Locate every blood parasite and identify its species.
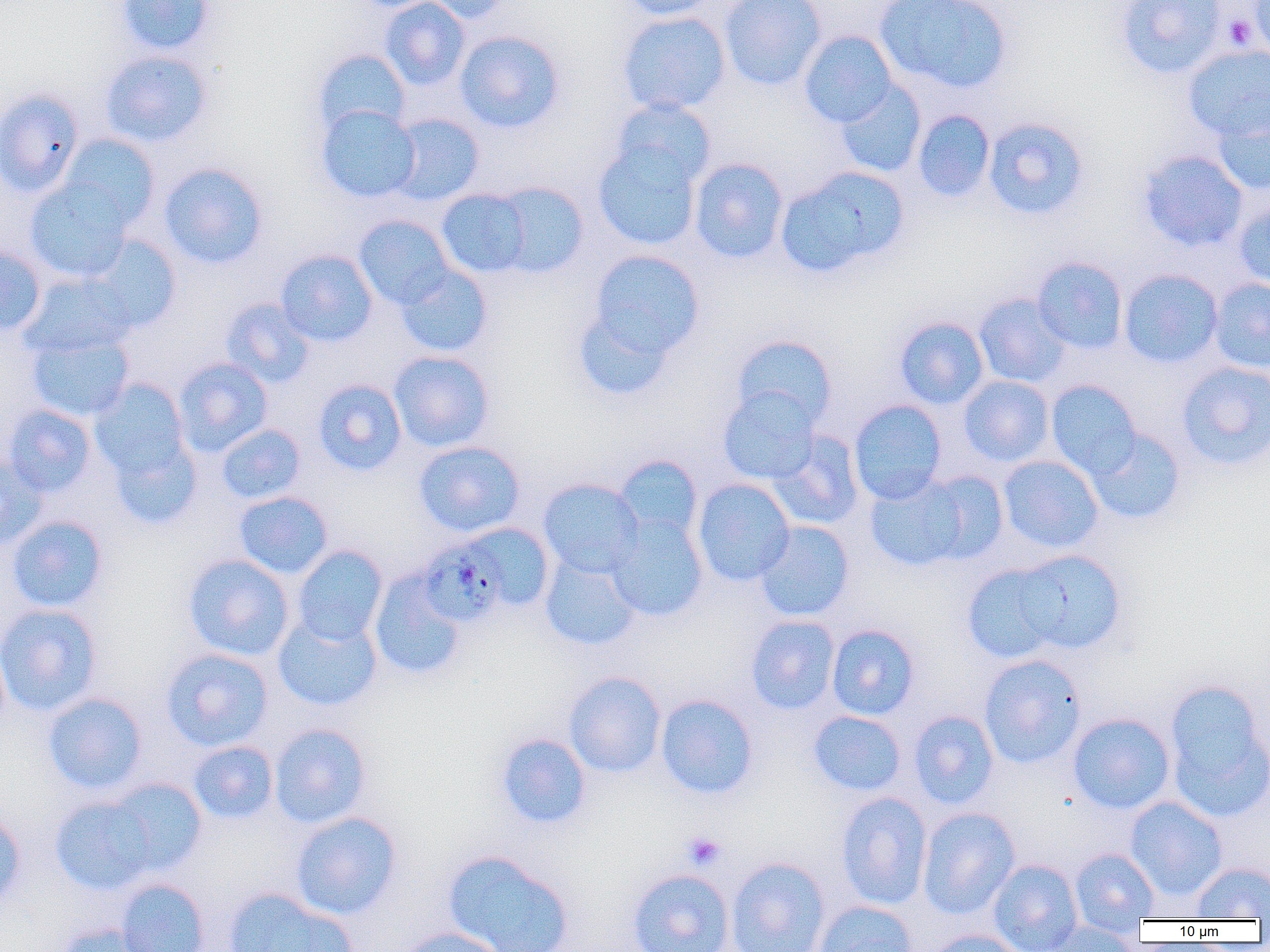
Approximate bounding boxes as [x1, y1, x2, y2] in pixels.
Plasmodium malariae-infected red blood cells: [425, 542, 506, 622].
No Plasmodium falciparum, Plasmodium ovale, Plasmodium vivax, Babesia divergens, or Trypanosoma brucei observed.

Platelet locations: [1224, 13, 1256, 51], [682, 832, 727, 870]. Uninfected red blood cell locations: [115, 0, 216, 56], [380, 0, 470, 90], [422, 0, 515, 23], [619, 0, 723, 20], [719, 0, 827, 91], [874, 0, 1012, 93], [1114, 0, 1229, 79], [1248, 0, 1270, 61], [616, 11, 732, 115], [454, 30, 565, 133], [799, 30, 897, 127], [1183, 44, 1270, 143], [312, 48, 410, 137], [100, 50, 212, 147], [835, 82, 926, 178], [0, 87, 86, 196], [611, 98, 717, 189], [1210, 98, 1269, 195], [835, 100, 996, 190], [316, 105, 421, 202], [912, 109, 995, 202], [389, 113, 485, 205], [983, 117, 1091, 220], [59, 134, 161, 230], [593, 142, 702, 250], [1138, 149, 1248, 252], [689, 157, 789, 263], [159, 162, 268, 269], [777, 166, 909, 276], [25, 178, 132, 282], [487, 181, 590, 278], [435, 187, 535, 278], [1234, 200, 1270, 291], [354, 215, 455, 308], [85, 235, 181, 331], [0, 244, 46, 335], [275, 249, 378, 347], [585, 250, 704, 364], [4, 255, 85, 351], [1031, 257, 1128, 354], [395, 263, 493, 357], [1119, 268, 1224, 368], [19, 272, 136, 358], [1209, 278, 1270, 372], [974, 293, 1073, 388], [220, 297, 315, 388], [573, 306, 680, 399], [894, 317, 989, 409], [27, 330, 135, 422], [732, 334, 837, 430], [389, 350, 494, 452], [173, 358, 273, 456], [1176, 361, 1270, 471], [958, 375, 1054, 466], [90, 378, 192, 482], [313, 378, 407, 476], [1046, 379, 1141, 477], [718, 387, 821, 484], [849, 399, 948, 504], [2, 404, 97, 497], [216, 424, 306, 504], [1086, 428, 1187, 525], [767, 430, 865, 529], [108, 432, 203, 529], [413, 440, 525, 537], [0, 455, 47, 551], [614, 455, 703, 544], [998, 455, 1103, 553], [864, 472, 980, 572], [538, 478, 644, 577], [693, 478, 795, 586], [234, 491, 333, 579], [606, 513, 708, 622], [7, 516, 108, 612], [753, 521, 855, 621], [456, 523, 554, 614], [292, 545, 388, 645], [1012, 549, 1127, 655], [182, 553, 294, 660], [540, 553, 641, 650], [961, 561, 1066, 663], [368, 570, 467, 680], [0, 603, 103, 717], [273, 612, 382, 711], [745, 615, 840, 715], [826, 624, 920, 720], [160, 648, 273, 751], [979, 654, 1087, 768], [564, 671, 666, 777], [1162, 678, 1270, 820], [43, 692, 148, 795], [655, 694, 758, 799], [808, 710, 906, 796], [908, 710, 1000, 809], [1067, 712, 1175, 814], [269, 723, 371, 828], [496, 733, 591, 829], [188, 740, 278, 824], [106, 777, 208, 875], [835, 792, 933, 909], [50, 795, 158, 894], [1125, 796, 1228, 901], [917, 807, 1021, 919], [0, 809, 27, 911], [290, 811, 402, 920], [1070, 847, 1159, 930], [442, 849, 575, 952], [726, 857, 831, 952], [988, 858, 1083, 951], [1190, 861, 1270, 919], [627, 868, 735, 952], [116, 878, 210, 952], [223, 888, 353, 952], [813, 900, 918, 952], [1037, 921, 1143, 951], [55, 922, 153, 952], [395, 926, 511, 952], [924, 928, 1029, 952]. Slide-level diagnosis: Plasmodium malariae. Image is 1270×952 pixels. Thin blood film. 1000x magnification. Optical microscopy. Single field of view.